Describe the morphology of the red blood cells.
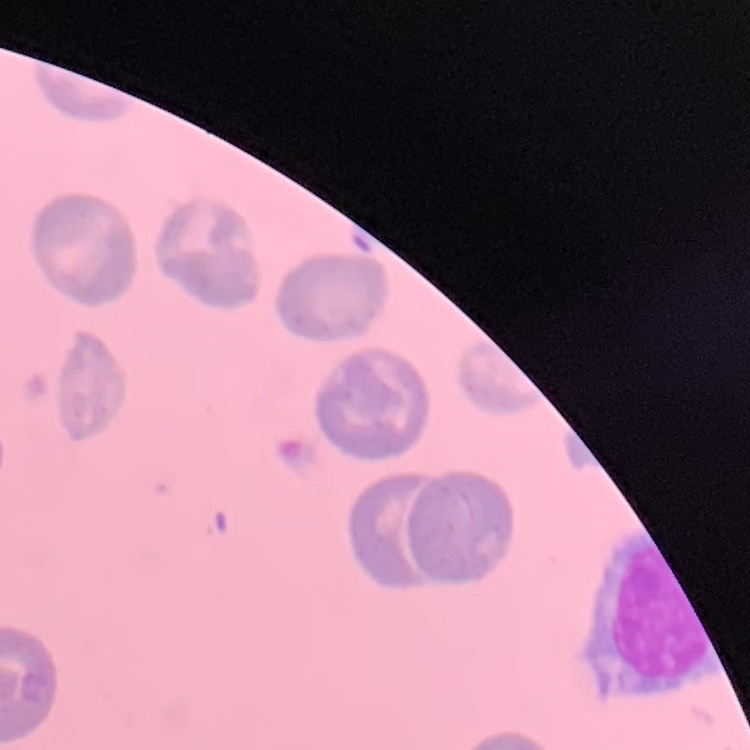

No rouleaux formation.

Summary:
  - Stain: Field's or Giemsa
  - Image type: square crop of a larger photomicrograph
  - Preparation: thin blood smear